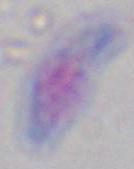
modality = micrograph
magnification = 1000x
identification = Toxoplasma gondii